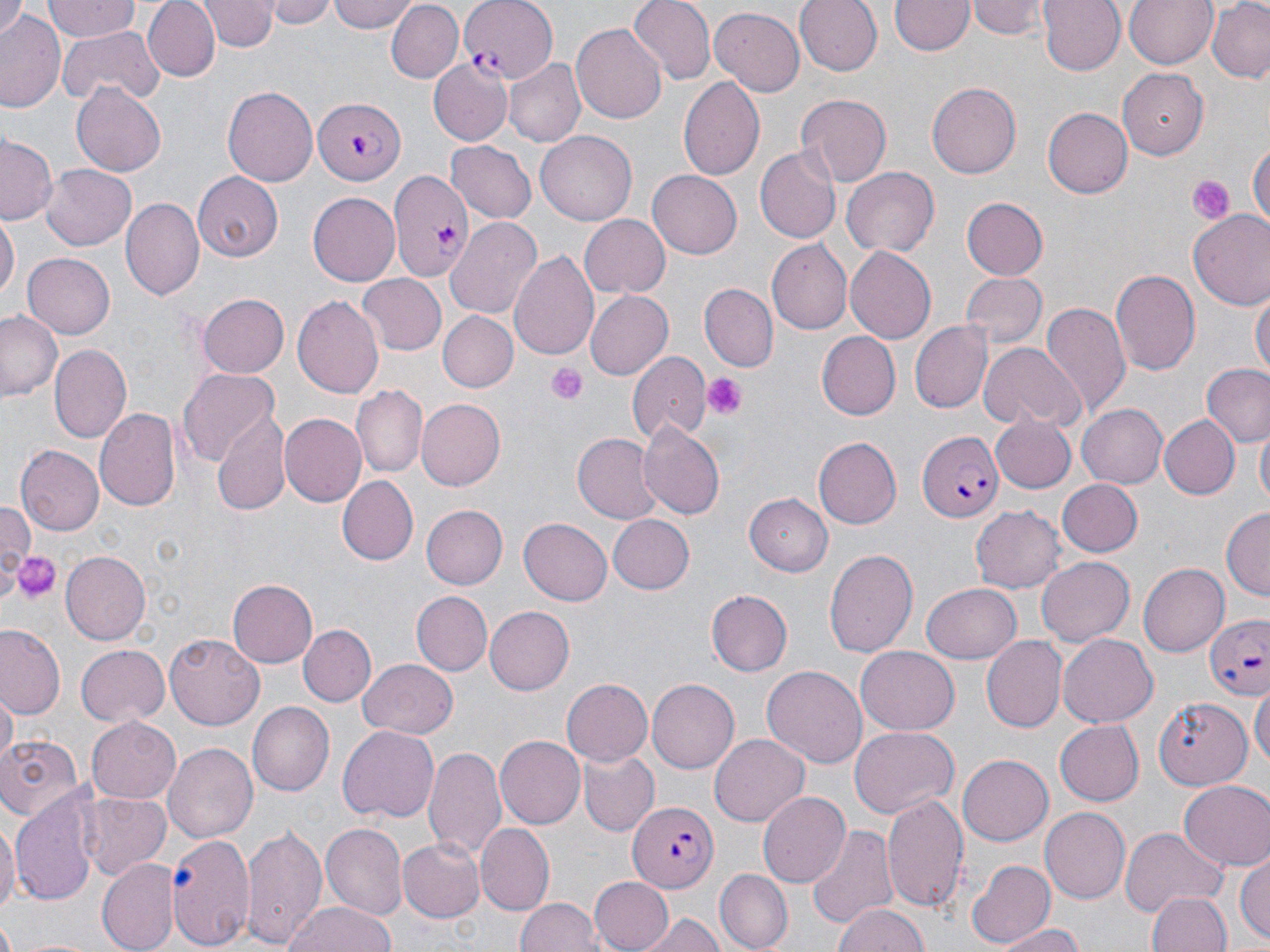

Summary:
  - Coordinate format: approximate bounding boxes as (x1,y1)-(x2,y2) corner pairs in pixels
  - Platelet locations: (1187,175)-(1236,221), (546,363)-(586,404), (702,371)-(744,416), (13,551)-(60,606)
  - Uninfected red blood cell locations: (44,0)-(137,43), (142,0)-(221,82), (203,0)-(274,51), (262,0)-(337,27), (328,0)-(418,33), (627,0)-(715,86), (794,0)-(880,75), (972,0)-(1045,38), (1039,0)-(1127,75), (1122,0)-(1216,69), (893,1)-(972,56), (1207,1)-(1270,83), (385,2)-(462,84), (0,5)-(25,40), (709,6)-(806,94), (1,9)-(63,109), (570,21)-(668,124), (57,26)-(160,108), (504,59)-(585,148), (428,60)-(512,146), (1118,70)-(1210,161), (679,74)-(765,181), (928,82)-(1022,178), (73,83)-(166,176), (225,83)-(319,187), (795,95)-(890,186), (1041,107)-(1131,199), (537,130)-(638,225), (1,134)-(58,225), (1249,137)-(1269,235), (447,139)-(536,224), (756,145)-(841,243), (40,165)-(136,250), (841,167)-(940,259), (646,169)-(742,258), (192,172)-(283,260), (308,192)-(400,284), (961,197)-(1048,281), (122,198)-(204,301), (1188,210)-(1270,312), (0,213)-(18,304), (581,215)-(670,297), (446,219)-(543,319), (767,241)-(853,333), (509,247)-(602,363), (846,247)-(936,345), (22,253)-(116,339), (1110,270)-(1201,377), (959,273)-(1047,350), (357,275)-(447,355), (698,283)-(778,372), (1251,286)-(1269,376), (583,288)-(673,378), (198,293)-(289,378), (293,295)-(385,401), (1041,302)-(1132,420), (0,310)-(64,402), (440,312)-(516,392), (911,323)-(990,413), (818,331)-(902,420), (978,342)-(1085,431), (50,345)-(131,444), (628,353)-(709,447), (1202,366)-(1270,451), (178,368)-(280,470), (351,386)-(427,478), (417,398)-(506,489), (1078,404)-(1166,487), (93,407)-(180,511), (213,411)-(289,513), (280,413)-(366,505), (992,413)-(1078,493), (1157,413)-(1240,501), (638,421)-(725,520), (1255,426)-(1270,504), (573,433)-(660,522), (815,437)-(903,529), (16,445)-(104,534), (336,476)-(417,566), (1057,479)-(1144,557), (742,493)-(832,577), (0,503)-(33,572), (424,504)-(507,589), (970,504)-(1066,592), (1220,507)-(1270,599), (608,515)-(694,593), (518,518)-(611,606), (825,548)-(917,659), (59,551)-(149,645), (1036,554)-(1135,646), (1137,562)-(1229,658), (229,578)-(318,669), (922,583)-(1023,663), (706,589)-(793,676), (410,591)-(491,676), (484,606)-(574,695), (299,624)-(376,707), (1,627)-(65,719), (166,631)-(263,726), (1057,634)-(1158,728), (979,635)-(1066,731), (75,645)-(170,727), (857,645)-(959,734), (358,657)-(457,738), (761,664)-(868,769), (561,678)-(652,767), (646,679)-(740,774), (1253,682)-(1268,776), (2,689)-(17,766), (1150,695)-(1251,796), (248,702)-(334,796), (85,716)-(180,803), (1055,721)-(1144,804), (852,725)-(960,817), (338,726)-(439,825), (0,734)-(83,824), (709,734)-(808,826), (497,735)-(588,829), (162,740)-(257,844), (425,746)-(508,863), (580,748)-(658,835), (959,756)-(1053,844), (1178,779)-(1270,871), (75,790)-(172,879), (756,792)-(849,887), (12,795)-(99,907), (883,795)-(970,915), (1040,808)-(1130,904), (0,817)-(18,921), (806,822)-(899,929), (475,823)-(554,915), (241,825)-(327,948), (320,825)-(406,919), (1119,827)-(1228,917), (169,833)-(256,951), (399,838)-(485,922), (1235,851)-(1270,947), (965,857)-(1054,950), (97,859)-(180,951), (714,870)-(793,952), (589,875)-(674,951), (1149,891)-(1230,952), (516,897)-(602,952), (283,900)-(397,952), (833,904)-(930,952), (638,911)-(726,951), (992,924)-(1089,952), (9,935)-(108,952)
  - Plasmodium falciparum-infected red blood cell locations: (460,0)-(556,81), (310,96)-(405,184), (393,170)-(475,282), (917,432)-(1003,521), (1206,616)-(1270,702), (627,802)-(719,891)
  - Slide-level diagnosis: Plasmodium falciparum
  - Field of view: one of a larger specimen
  - Preparation: thin blood smear
  - Magnification: 1000x
  - Modality: optical microscopy
  - Stain: May-Grünwald-Giemsa
  - Image size: 1270×952 pixels